Describe the morphology of the red blood cells.
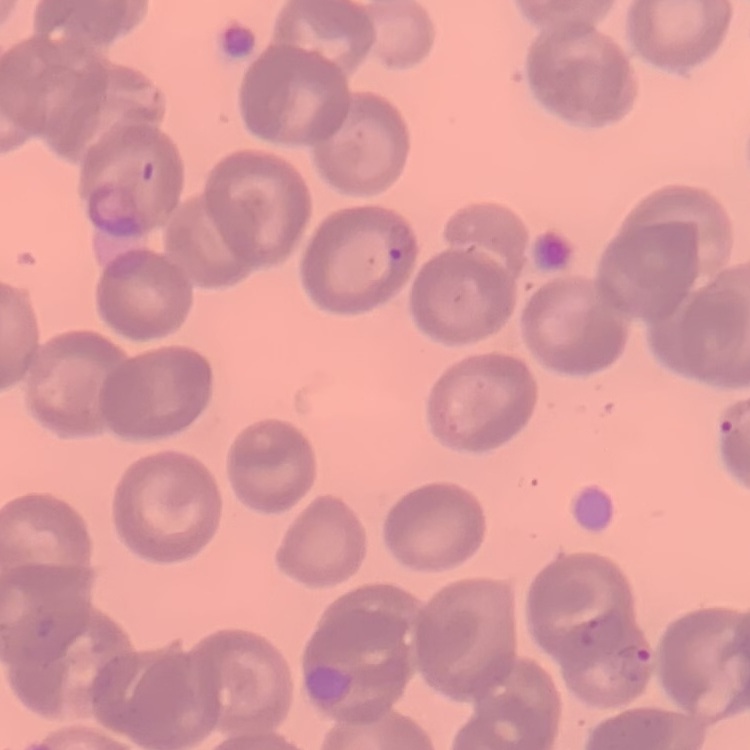
They show no rouleaux formation.

Summary:
  - Preparation: thin blood smear
  - Image type: one tile cut from a larger photomicrograph
  - Stain: Field's or Giemsa